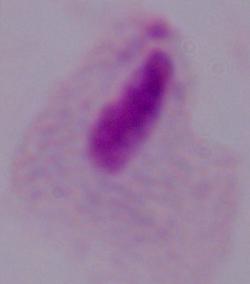 Micrograph. Captured at 1000x magnification. A trichomonad is shown.